State which parasite is depicted.
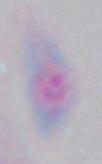
Toxoplasma gondii.

modality: micrograph
magnification: 1000x